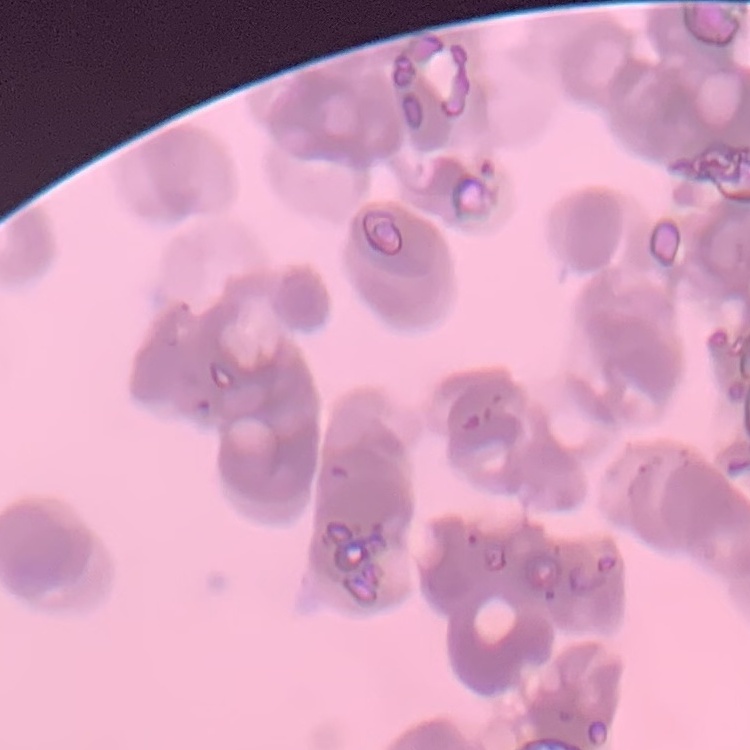
Summary:
  - Red blood cell morphology: rouleaux formation
  - Image type: square crop of a larger photomicrograph
  - Preparation: thin blood film
  - Stain: Field's or Giemsa